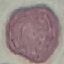
Summary:
  - Result: no malaria parasites detected
  - Capture: smartphone camera at the microscope eyepiece
  - Image type: cell patch, automatically extracted from a larger field of view and resized to 64 × 64 pixels
  - Preparation: thin smear
  - Stain: Giemsa